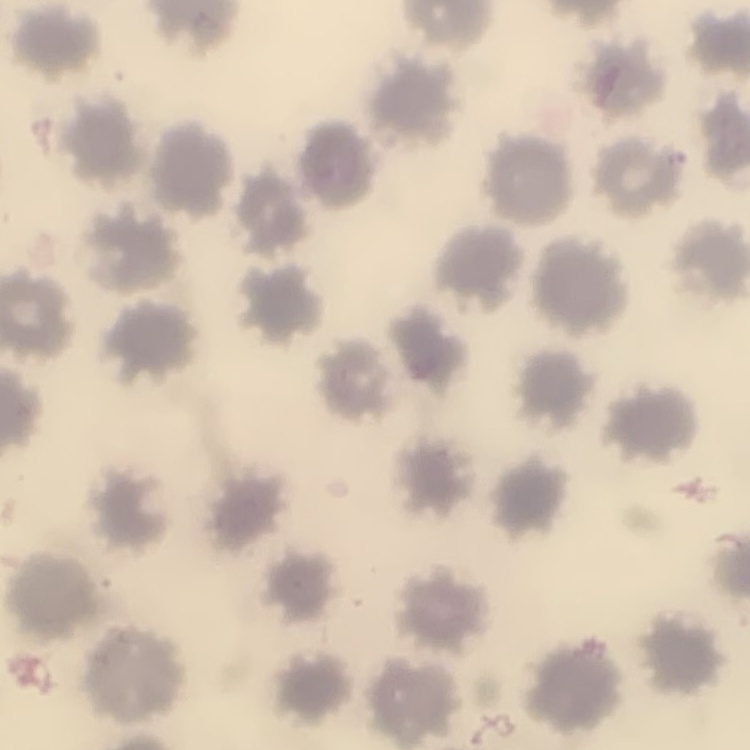
The red blood cells exhibit no rouleaux formation. Thin blood film. Square crop of a larger photomicrograph. Stained with either Field's or Giemsa.